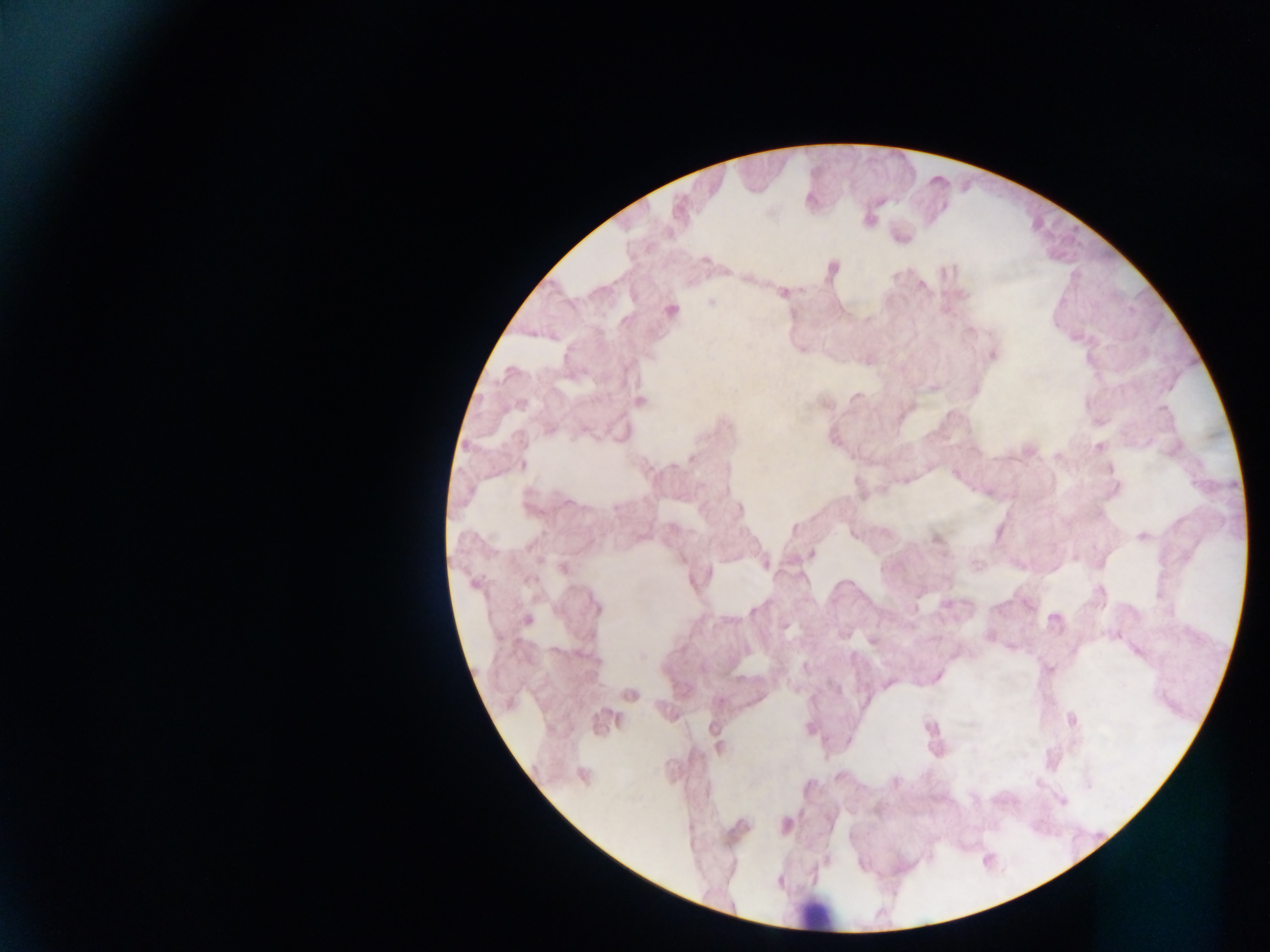
Approximate centers as [x, y] in pixels. Leukocyte locations: [817, 916]. Collected in Ghana. Mobile-phone photograph taken through the microscope. Image is 1270×952 pixels. Thick blood smear. Single field of view.